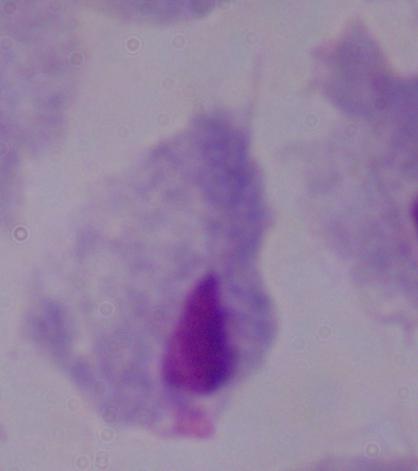

{
  "identification": "trichomonad",
  "modality": "micrograph",
  "magnification": "1000x"
}